Locate every Plasmodium falciparum-infected red blood cell.
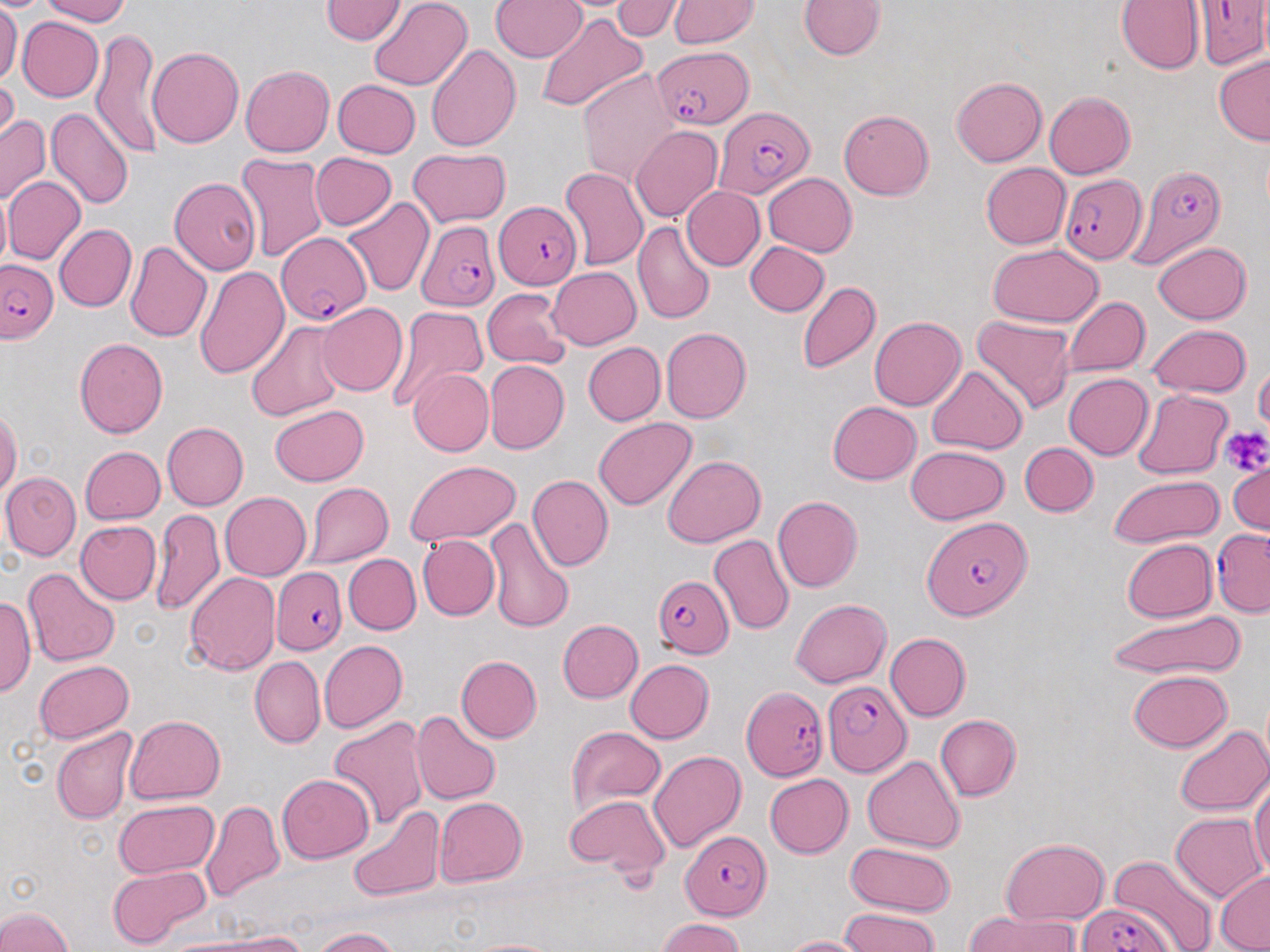

Approximate bounding boxes as named x1/y1/x2/y2 corners in pixels.
Plasmodium falciparum-infected red blood cells: (x1=1193, y1=0, x2=1270, y2=69), (x1=656, y1=44, x2=754, y2=129), (x1=716, y1=107, x2=813, y2=198), (x1=1130, y1=164, x2=1226, y2=266), (x1=1061, y1=171, x2=1147, y2=262), (x1=497, y1=200, x2=584, y2=291), (x1=415, y1=220, x2=499, y2=311), (x1=277, y1=234, x2=372, y2=326), (x1=1, y1=259, x2=57, y2=344), (x1=922, y1=514, x2=1030, y2=618), (x1=1212, y1=530, x2=1270, y2=615), (x1=272, y1=567, x2=348, y2=654), (x1=653, y1=577, x2=733, y2=657), (x1=823, y1=679, x2=909, y2=776), (x1=742, y1=688, x2=827, y2=781), (x1=683, y1=833, x2=773, y2=919), (x1=1076, y1=902, x2=1170, y2=952).

Platelet locations: (x1=1221, y1=425, x2=1270, y2=474). Uninfected red blood cell locations: (x1=39, y1=0, x2=131, y2=25), (x1=319, y1=0, x2=406, y2=45), (x1=368, y1=0, x2=474, y2=90), (x1=613, y1=0, x2=683, y2=40), (x1=799, y1=0, x2=887, y2=59), (x1=1116, y1=0, x2=1205, y2=74), (x1=490, y1=1, x2=587, y2=62), (x1=667, y1=1, x2=758, y2=49), (x1=0, y1=2, x2=22, y2=88), (x1=534, y1=13, x2=648, y2=114), (x1=17, y1=16, x2=103, y2=102), (x1=92, y1=27, x2=163, y2=158), (x1=425, y1=44, x2=522, y2=152), (x1=148, y1=47, x2=244, y2=149), (x1=1213, y1=55, x2=1270, y2=144), (x1=240, y1=65, x2=334, y2=156), (x1=578, y1=69, x2=681, y2=185), (x1=0, y1=73, x2=19, y2=155), (x1=950, y1=77, x2=1047, y2=167), (x1=332, y1=80, x2=421, y2=159), (x1=1044, y1=91, x2=1135, y2=178), (x1=46, y1=106, x2=133, y2=212), (x1=837, y1=110, x2=934, y2=199), (x1=0, y1=115, x2=51, y2=207), (x1=630, y1=126, x2=721, y2=224), (x1=408, y1=148, x2=511, y2=227), (x1=310, y1=152, x2=396, y2=230), (x1=235, y1=153, x2=329, y2=262), (x1=980, y1=163, x2=1071, y2=249), (x1=560, y1=166, x2=649, y2=270), (x1=763, y1=173, x2=857, y2=257), (x1=5, y1=177, x2=87, y2=265), (x1=169, y1=178, x2=261, y2=276), (x1=681, y1=185, x2=765, y2=271), (x1=0, y1=188, x2=11, y2=277), (x1=343, y1=198, x2=434, y2=296), (x1=633, y1=222, x2=714, y2=325), (x1=54, y1=224, x2=136, y2=312), (x1=124, y1=240, x2=212, y2=342), (x1=1153, y1=241, x2=1251, y2=323), (x1=745, y1=242, x2=829, y2=316), (x1=988, y1=244, x2=1103, y2=327), (x1=195, y1=264, x2=290, y2=379), (x1=548, y1=266, x2=642, y2=350), (x1=797, y1=280, x2=880, y2=375), (x1=482, y1=288, x2=571, y2=369), (x1=1063, y1=297, x2=1150, y2=378), (x1=316, y1=303, x2=408, y2=396), (x1=386, y1=305, x2=490, y2=413), (x1=971, y1=313, x2=1075, y2=412), (x1=869, y1=316, x2=965, y2=409), (x1=246, y1=321, x2=345, y2=422), (x1=1149, y1=324, x2=1252, y2=398), (x1=661, y1=327, x2=751, y2=423), (x1=74, y1=337, x2=169, y2=438), (x1=583, y1=342, x2=665, y2=425), (x1=484, y1=360, x2=570, y2=455), (x1=1254, y1=362, x2=1270, y2=435), (x1=927, y1=365, x2=1027, y2=453), (x1=407, y1=368, x2=494, y2=457), (x1=1063, y1=373, x2=1153, y2=460), (x1=1132, y1=389, x2=1235, y2=479), (x1=828, y1=401, x2=921, y2=485), (x1=271, y1=404, x2=368, y2=486), (x1=0, y1=408, x2=20, y2=499), (x1=593, y1=418, x2=696, y2=511), (x1=162, y1=422, x2=249, y2=510), (x1=1020, y1=442, x2=1098, y2=516), (x1=906, y1=445, x2=1010, y2=524), (x1=80, y1=446, x2=166, y2=524), (x1=662, y1=456, x2=766, y2=548), (x1=1228, y1=459, x2=1268, y2=536), (x1=405, y1=460, x2=521, y2=545), (x1=1, y1=471, x2=81, y2=560), (x1=1108, y1=474, x2=1223, y2=548), (x1=527, y1=475, x2=614, y2=571), (x1=304, y1=481, x2=394, y2=567), (x1=220, y1=492, x2=311, y2=580), (x1=773, y1=496, x2=863, y2=592), (x1=152, y1=508, x2=225, y2=617), (x1=485, y1=516, x2=574, y2=634), (x1=74, y1=520, x2=161, y2=604), (x1=417, y1=534, x2=499, y2=621), (x1=709, y1=534, x2=794, y2=634), (x1=1122, y1=539, x2=1216, y2=622), (x1=344, y1=554, x2=421, y2=635), (x1=23, y1=567, x2=120, y2=666), (x1=184, y1=572, x2=281, y2=675), (x1=1, y1=593, x2=36, y2=698), (x1=790, y1=598, x2=891, y2=688), (x1=1107, y1=610, x2=1249, y2=680), (x1=556, y1=620, x2=643, y2=703), (x1=885, y1=632, x2=971, y2=721), (x1=319, y1=640, x2=407, y2=732), (x1=250, y1=655, x2=325, y2=748), (x1=455, y1=655, x2=542, y2=743), (x1=625, y1=659, x2=713, y2=744), (x1=34, y1=661, x2=133, y2=744), (x1=1128, y1=670, x2=1232, y2=750), (x1=411, y1=711, x2=501, y2=805), (x1=934, y1=714, x2=1021, y2=801), (x1=124, y1=715, x2=225, y2=805), (x1=329, y1=715, x2=429, y2=829), (x1=566, y1=725, x2=665, y2=817), (x1=1173, y1=725, x2=1269, y2=816), (x1=52, y1=727, x2=137, y2=824), (x1=648, y1=750, x2=745, y2=853), (x1=862, y1=754, x2=966, y2=853), (x1=277, y1=774, x2=373, y2=863), (x1=764, y1=774, x2=854, y2=859), (x1=1250, y1=774, x2=1270, y2=879), (x1=565, y1=794, x2=670, y2=878), (x1=434, y1=796, x2=526, y2=886), (x1=113, y1=799, x2=219, y2=877), (x1=201, y1=801, x2=284, y2=904), (x1=348, y1=807, x2=445, y2=903), (x1=1171, y1=812, x2=1264, y2=901), (x1=1000, y1=838, x2=1109, y2=925), (x1=845, y1=842, x2=956, y2=916), (x1=1109, y1=853, x2=1217, y2=952), (x1=108, y1=864, x2=209, y2=948), (x1=1215, y1=871, x2=1270, y2=950), (x1=0, y1=906, x2=71, y2=952), (x1=840, y1=908, x2=940, y2=951), (x1=965, y1=910, x2=1078, y2=952), (x1=656, y1=918, x2=744, y2=952), (x1=311, y1=926, x2=400, y2=952), (x1=209, y1=930, x2=312, y2=951), (x1=780, y1=935, x2=868, y2=952), (x1=464, y1=937, x2=566, y2=952). Slide-level diagnosis: Plasmodium falciparum. One field of a larger specimen. Light microscopy. May-Grünwald-Giemsa stain. Thin blood film. Captured at 1000x magnification. Image is 1270×952 pixels.